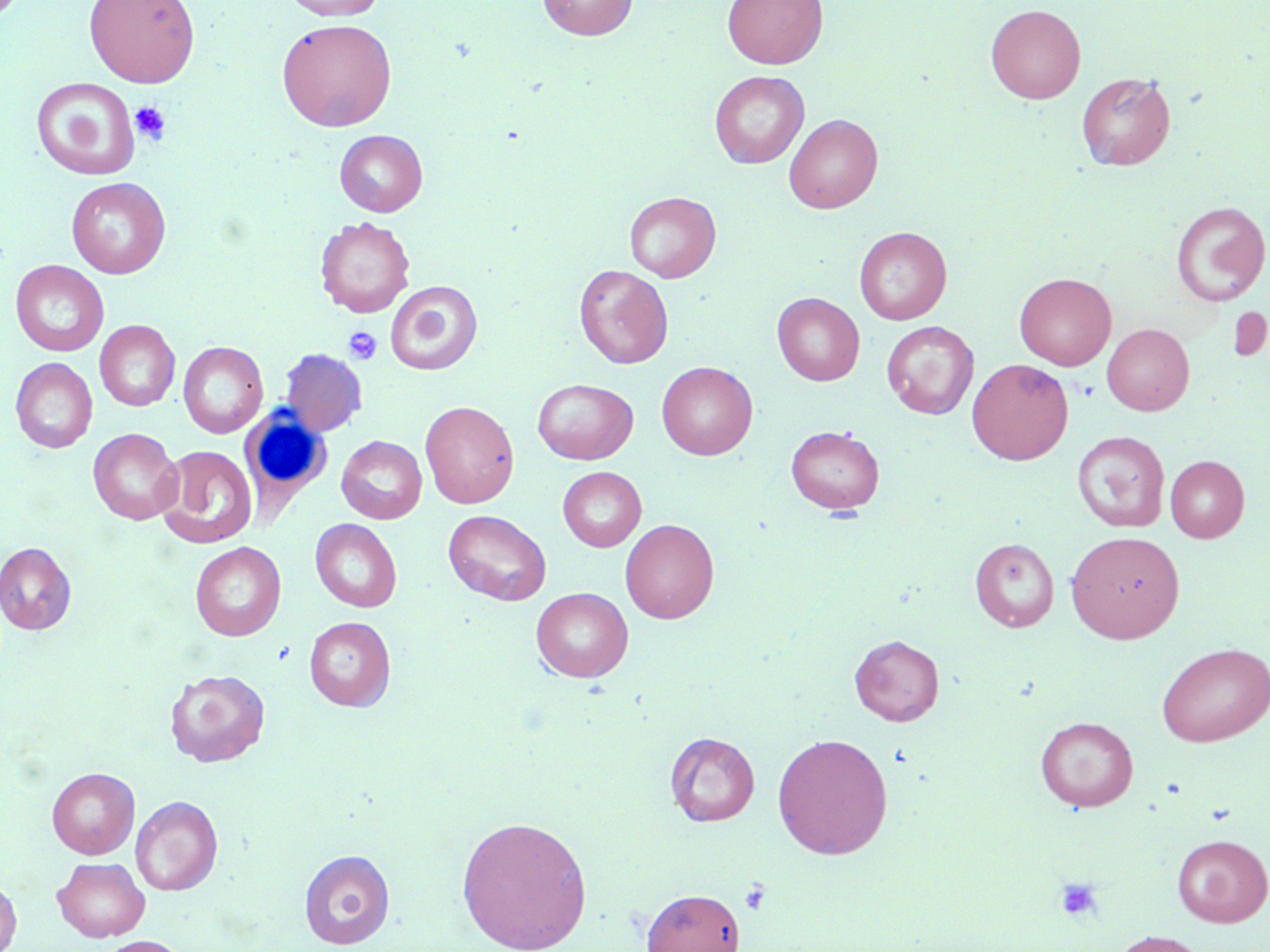
Approximate bounding boxes as (x1, y1, x2, y2) in pixels. Uninfected red blood cell locations (subset): (83, 0, 200, 88), (282, 0, 388, 20), (536, 0, 637, 40), (722, 0, 827, 69), (986, 4, 1086, 103), (276, 18, 397, 132), (709, 70, 809, 168), (1076, 72, 1175, 170), (31, 78, 140, 180), (784, 114, 883, 213), (334, 130, 428, 216), (66, 177, 171, 278), (624, 192, 721, 282), (1170, 201, 1269, 306), (315, 216, 416, 318), (854, 227, 951, 325), (10, 260, 108, 357), (574, 264, 673, 368), (1014, 272, 1116, 370), (385, 280, 483, 375), (772, 293, 864, 385), (95, 320, 180, 411), (881, 321, 979, 419), (1102, 323, 1194, 415), (178, 341, 268, 438), (279, 348, 367, 436), (10, 357, 97, 453), (966, 358, 1073, 464), (657, 361, 757, 460), (532, 378, 638, 464), (420, 400, 519, 508), (785, 425, 885, 514), (88, 428, 183, 525), (1072, 431, 1170, 532), (337, 435, 427, 524), (155, 445, 258, 548), (1165, 455, 1249, 542), (558, 467, 646, 552), (443, 510, 551, 606), (311, 519, 402, 612), (620, 519, 719, 623), (1066, 531, 1184, 643), (970, 537, 1059, 631), (0, 542, 76, 634), (190, 542, 286, 641), (531, 587, 633, 682), (304, 616, 395, 710), (849, 634, 944, 725), (1156, 642, 1270, 746), (165, 669, 270, 767), (1035, 716, 1138, 812), (665, 731, 760, 826), (772, 732, 893, 859), (46, 767, 139, 859), (130, 795, 223, 895), (456, 815, 592, 952), (1171, 833, 1270, 927), (299, 849, 395, 948), (52, 857, 150, 941), (0, 878, 21, 952), (641, 887, 746, 952), (1108, 931, 1212, 952), (94, 935, 191, 952). Platelet locations (subset): (129, 102, 171, 144), (343, 327, 382, 365), (1055, 876, 1104, 923), (739, 880, 773, 915). White blood cell locations: (240, 411, 333, 512). Slide-level diagnosis: no evidence of blood parasites. Optical microscopy. One field of a larger specimen. 1000x magnification. Thin blood film. May-Grünwald-Giemsa-stained preparation. Image is 1270×952 pixels.